Locate and identify every blood parasite.
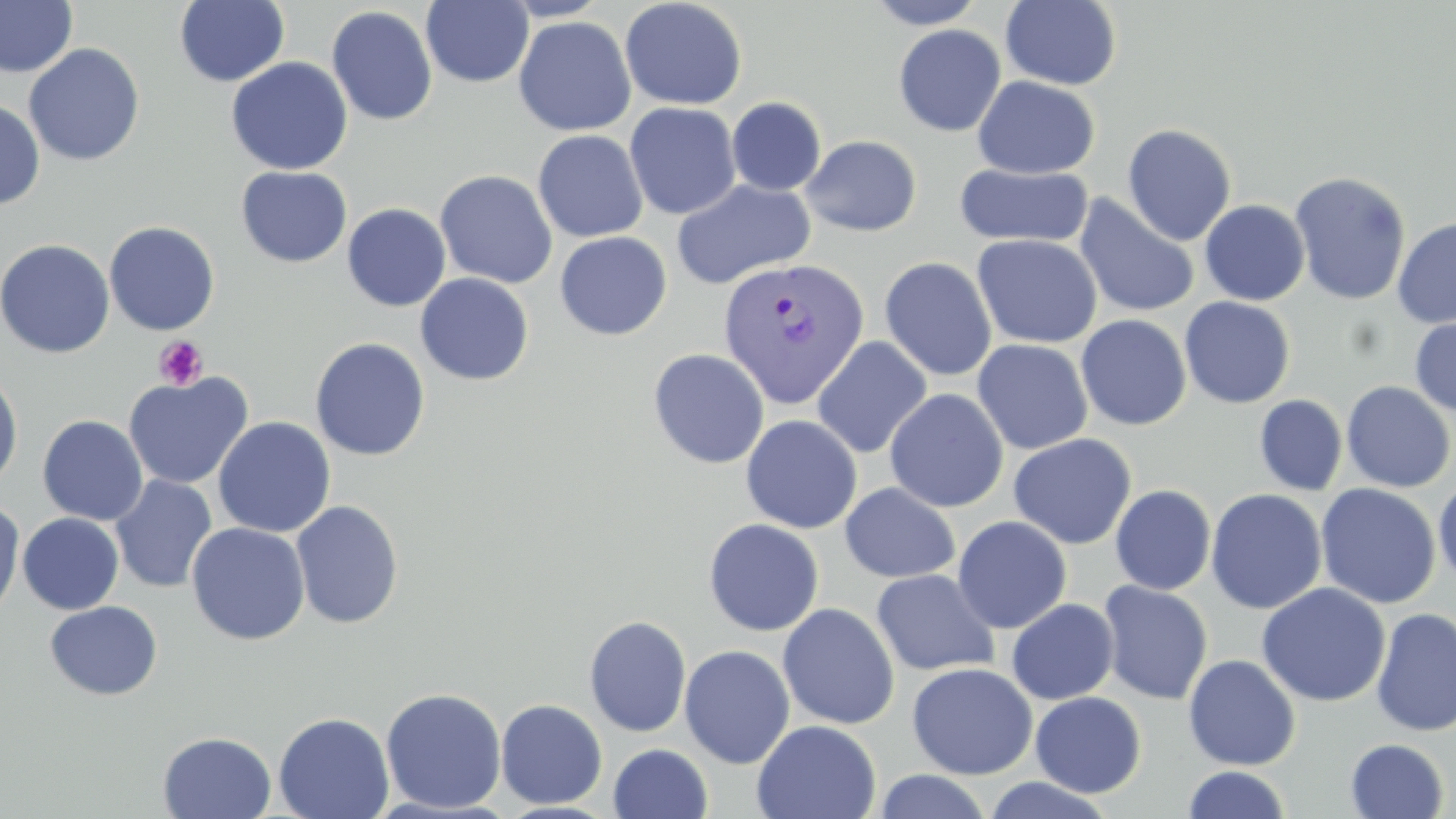
Approximate bounding boxes as (x1,y1)-(x2,y2) corner pairs in pixels.
Plasmodium vivax-infected red blood cells: (716,257)-(870,409).
No Plasmodium falciparum, Plasmodium ovale, Plasmodium malariae, Babesia divergens, or Trypanosoma brucei observed.

Summary:
  - Uninfected red blood cell locations: (0,0)-(78,78), (619,0)-(748,110), (863,0)-(987,29), (1000,0)-(1123,90), (174,1)-(290,87), (421,1)-(534,88), (424,2)-(604,121), (326,6)-(438,126), (513,15)-(636,136), (893,24)-(1006,137), (24,43)-(145,166), (226,57)-(353,175), (973,76)-(1099,179), (726,97)-(827,196), (0,98)-(45,210), (624,102)-(741,220), (1122,123)-(1237,246), (532,130)-(648,243), (801,134)-(921,237), (955,163)-(1093,249), (236,166)-(352,268), (435,170)-(558,289), (1288,170)-(1412,306), (672,178)-(816,289), (1074,193)-(1200,319), (1199,199)-(1310,306), (342,203)-(451,312), (1392,216)-(1456,328), (104,221)-(220,336), (554,231)-(672,340), (972,234)-(1102,349), (0,238)-(115,359), (879,257)-(997,381), (415,273)-(534,386), (1179,296)-(1295,408), (1076,314)-(1192,431), (1409,316)-(1456,417), (812,336)-(932,459), (309,337)-(431,461), (972,339)-(1093,454), (648,348)-(769,469), (0,367)-(24,492), (123,371)-(254,489), (1341,381)-(1455,493), (884,388)-(1008,512), (1255,394)-(1348,496), (741,414)-(862,534), (37,415)-(149,526), (212,416)-(336,538), (1008,433)-(1136,550), (110,475)-(218,593), (1433,477)-(1456,585), (840,482)-(960,583), (1316,483)-(1441,609), (1110,485)-(1216,595), (1206,488)-(1327,614), (0,497)-(25,624), (290,500)-(405,629), (17,513)-(123,615), (952,515)-(1072,633), (703,518)-(824,636), (187,522)-(310,645), (871,569)-(1000,676), (1098,581)-(1213,704), (1256,583)-(1391,707), (1006,599)-(1119,704), (44,600)-(163,701), (777,603)-(900,730), (1371,606)-(1456,737), (584,615)-(692,737), (679,644)-(795,768), (1183,654)-(1302,770), (907,662)-(1038,779), (381,687)-(507,814), (1030,691)-(1146,797), (495,699)-(608,809), (273,711)-(394,819), (752,720)-(881,819), (158,731)-(276,818), (1345,738)-(1450,819), (608,743)-(712,819), (1181,765)-(1292,818), (872,770)-(993,819), (982,776)-(1116,818)
  - Platelet locations: (153,336)-(209,390)
  - Slide-level diagnosis: Plasmodium vivax
  - Stain: May-Grünwald-Giemsa
  - Modality: light microscopy
  - Preparation: thin blood smear
  - Magnification: 1000x
  - Field of view: one of a larger specimen
  - Image size: 1456×819 pixels